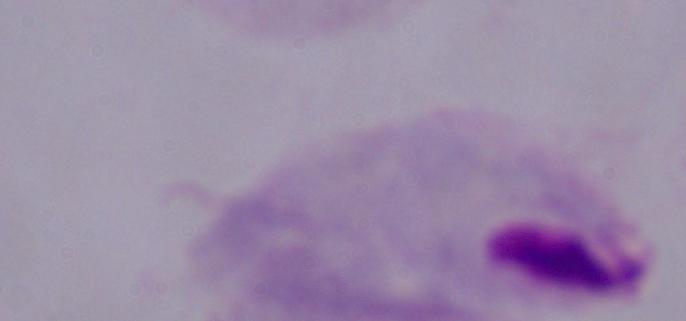

Summary:
  - Identification: trichomonad
  - Modality: photomicrograph
  - Magnification: 1000x